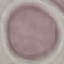
Malaria status: uninfected. Giemsa-stained preparation. Thin blood smear. Acquired by smartphone through the microscope eyepiece. Automatically extracted cell patch, resized to 64 × 64 pixels.